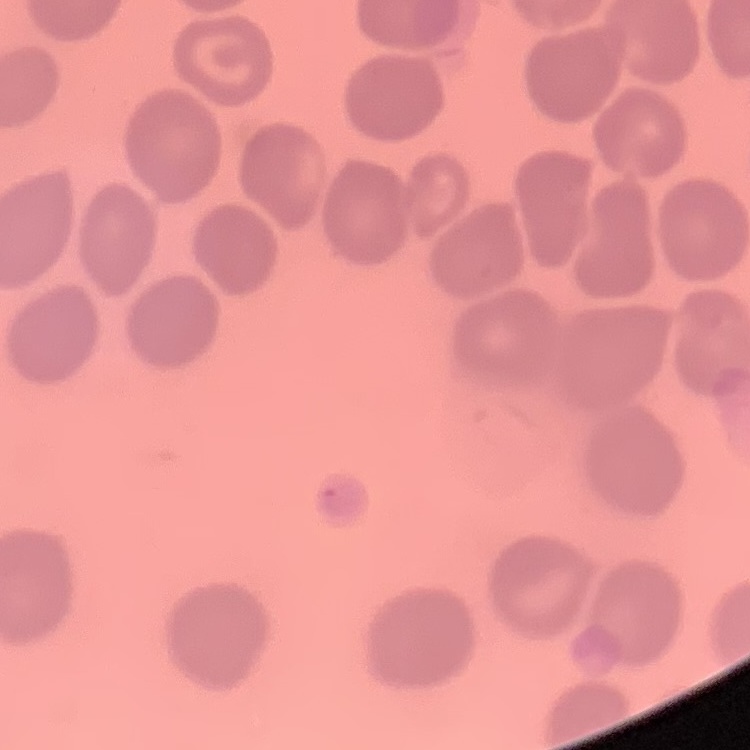

Summary:
  - Red blood cell morphology: no rouleaux formation
  - Image type: square crop of a larger photomicrograph
  - Preparation: thin blood film
  - Stain: Field's or Giemsa